Report the malaria status of this cell.
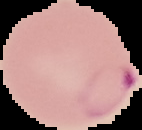
It is parasitized.

image_size: 142×130 pixels
image_type: segmented cell region on a black background
preparation: thin blood film